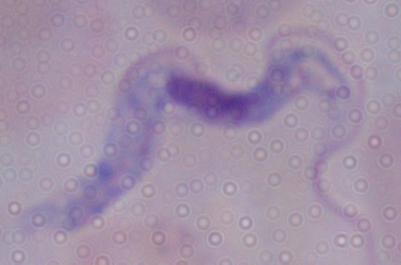

Summary:
  - Magnification: 1000x
  - Identification: trypanosome
  - Modality: photomicrograph